Report the malaria status of this cell.
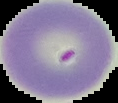

It is uninfected.

Summary:
  - Preparation: thin blood film
  - Image type: segmented cell region with the area outside set to black
  - Image size: 118×103 pixels